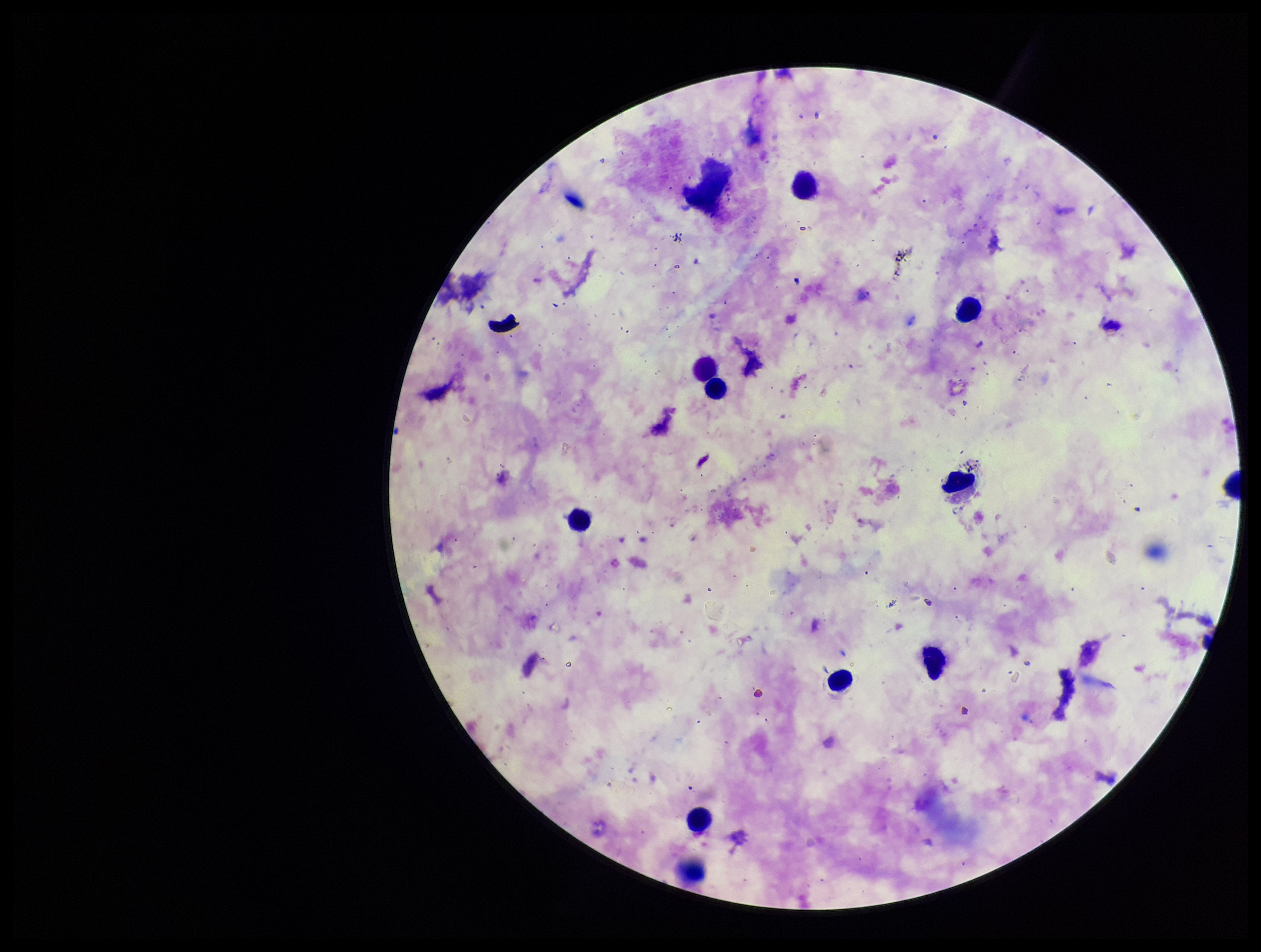
Photographed through the microscope eyepiece with a smartphone camera. Plasmodium parasites: none identified. Patient malaria status: infected. Species reported for this patient: Plasmodium falciparum. Giemsa stain. Image is 1261×952 pixels. Leukocyte count: 11. One field from this slide. Preparation: thick blood smear. Parasite count: 0.